Locate every blood parasite and identify its species.
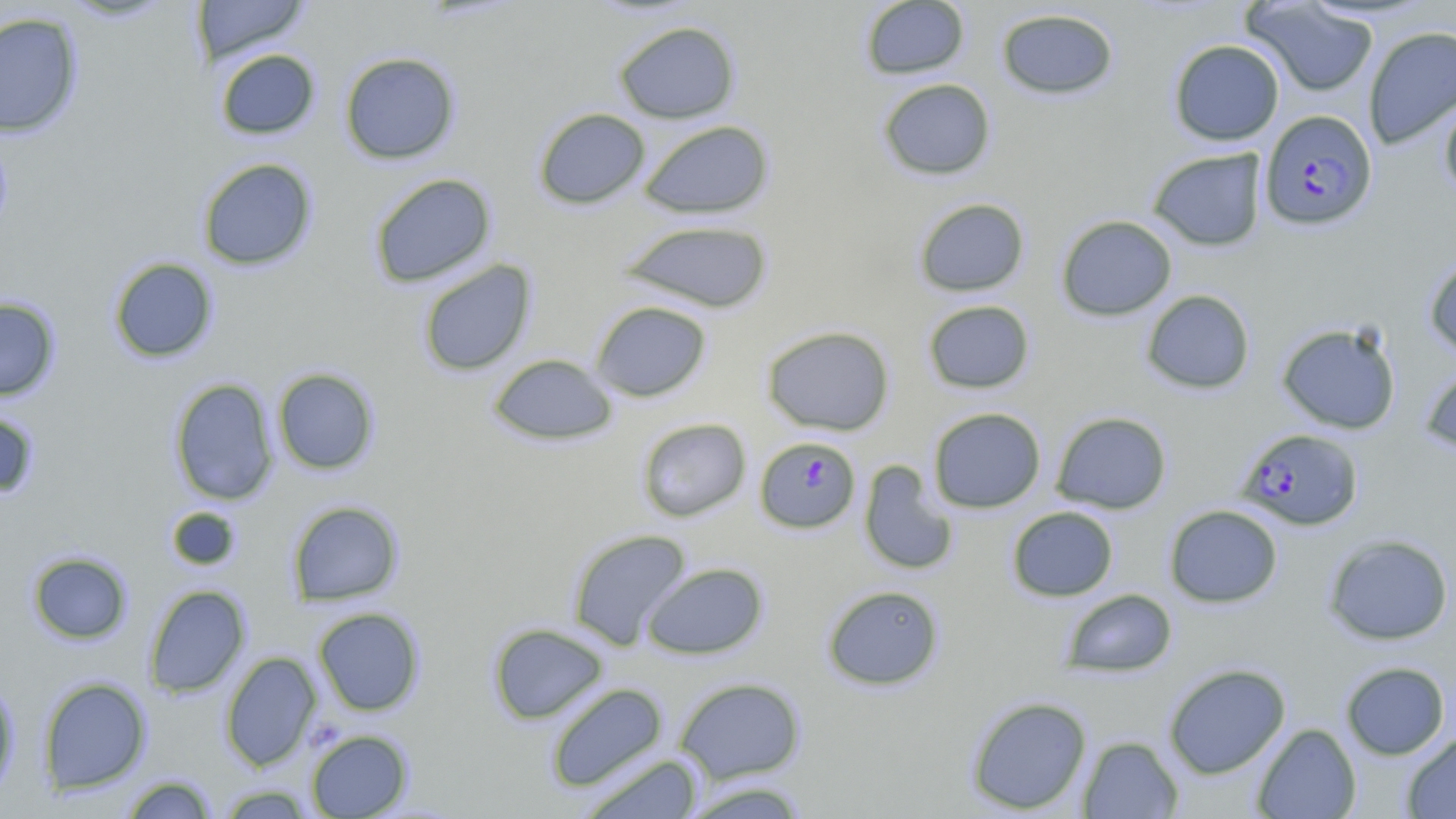
Approximate bounding boxes as (x1, y1, x2, y2) in pixels.
Plasmodium falciparum-infected red blood cells: (1260, 110, 1378, 230), (1236, 428, 1363, 530), (755, 436, 861, 534).
No Plasmodium ovale, Plasmodium malariae, Plasmodium vivax, Babesia divergens, or Trypanosoma brucei observed.

Uninfected red blood cell locations: (60, 0, 176, 22), (191, 0, 310, 65), (859, 1, 970, 80), (1242, 1, 1379, 97), (996, 8, 1119, 100), (0, 12, 84, 138), (613, 20, 740, 124), (1363, 25, 1456, 150), (1168, 39, 1284, 145), (215, 49, 320, 140), (339, 51, 461, 165), (877, 78, 996, 180), (1439, 92, 1456, 203), (533, 107, 650, 210), (638, 120, 775, 220), (1146, 147, 1268, 251), (197, 158, 318, 271), (369, 173, 497, 288), (913, 197, 1030, 297), (1055, 215, 1177, 321), (618, 219, 774, 314), (1423, 255, 1456, 360), (108, 257, 218, 363), (417, 259, 537, 377), (1140, 289, 1255, 394), (0, 297, 60, 401), (922, 300, 1035, 394), (591, 301, 711, 402), (1276, 322, 1402, 435), (761, 325, 895, 436), (488, 354, 617, 446), (1419, 364, 1456, 456), (272, 367, 380, 475), (169, 378, 279, 506), (928, 407, 1046, 513), (0, 408, 41, 500), (1051, 411, 1172, 514), (636, 417, 751, 522), (858, 460, 958, 576), (287, 500, 404, 606), (1164, 504, 1283, 608), (166, 506, 240, 571), (1006, 506, 1119, 602), (567, 528, 692, 650), (1323, 534, 1454, 645), (27, 551, 132, 644), (641, 562, 768, 659), (144, 584, 251, 698), (822, 584, 945, 690), (1061, 588, 1177, 678), (313, 607, 425, 715), (488, 622, 609, 725), (220, 651, 322, 771), (1340, 661, 1450, 760), (1163, 663, 1291, 779), (0, 675, 19, 801), (38, 676, 152, 794), (674, 677, 806, 783), (545, 682, 668, 792), (965, 695, 1092, 815), (1251, 723, 1361, 818), (306, 729, 413, 818), (1401, 731, 1456, 818), (1077, 735, 1184, 818), (579, 752, 705, 819), (120, 775, 218, 818), (679, 780, 812, 818), (214, 784, 317, 818). Slide-level diagnosis: Plasmodium falciparum. Image is 1456×819 pixels. Single field of view. Thin blood smear. Light microscopy. 1000x magnification. May-Grünwald-Giemsa stain.